Classify this cell by malaria status.
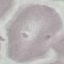

Uninfected.

Summary:
  - Stain: Giemsa
  - Preparation: thin smear
  - Capture: smartphone through the microscope eyepiece
  - Image type: cell patch, automatically extracted from a larger field of view and resized to 64 × 64 pixels